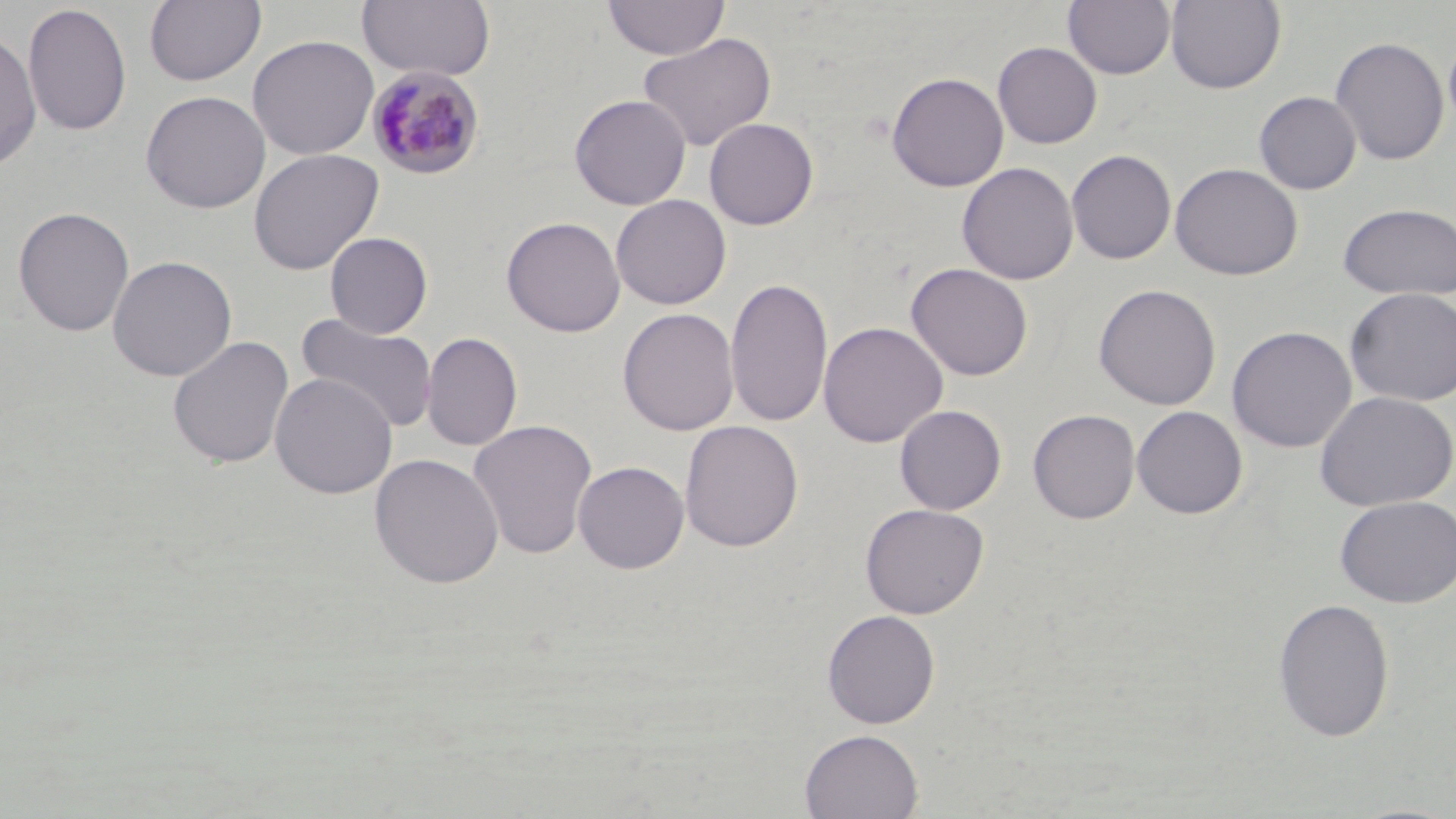
Summary:
  - Coordinate format: approximate bounding boxes as (x1, y1, x2, y2) in pixels
  - Plasmodium malariae-infected red blood cell locations: (367, 67, 484, 180)
  - Uninfected red blood cell locations: (144, 0, 266, 87), (357, 0, 496, 83), (603, 0, 729, 60), (1063, 0, 1175, 80), (1166, 0, 1286, 94), (22, 2, 132, 137), (1443, 29, 1456, 135), (0, 30, 42, 174), (637, 33, 776, 152), (247, 34, 379, 159), (1329, 36, 1450, 166), (993, 42, 1102, 148), (886, 71, 1009, 192), (140, 90, 271, 213), (1254, 91, 1361, 195), (569, 94, 691, 210), (704, 117, 818, 230), (248, 148, 384, 275), (1067, 149, 1177, 265), (957, 162, 1078, 285), (1169, 162, 1304, 281), (610, 194, 731, 310), (1337, 202, 1456, 300), (12, 206, 135, 337), (501, 216, 626, 338), (325, 232, 433, 338), (107, 255, 237, 382), (906, 263, 1034, 381), (725, 276, 833, 429), (1093, 283, 1222, 411), (1344, 288, 1456, 407), (617, 307, 739, 436), (295, 312, 439, 434), (818, 321, 947, 448), (1226, 325, 1357, 453), (421, 331, 523, 452), (167, 335, 295, 470), (270, 373, 398, 499), (1314, 390, 1456, 511), (894, 404, 1007, 515), (1131, 406, 1247, 520), (1027, 409, 1140, 524), (468, 418, 598, 560), (679, 420, 804, 552), (572, 447, 804, 566), (369, 452, 505, 589), (572, 460, 690, 574), (1335, 495, 1456, 608), (860, 503, 989, 618), (1272, 597, 1395, 743), (821, 609, 940, 729), (799, 729, 924, 818)
  - Slide-level diagnosis: Plasmodium malariae
  - Preparation: thin blood smear
  - Image size: 1456×819 pixels
  - Magnification: 1000x
  - Stain: May-Grünwald-Giemsa
  - Field of view: one of a larger specimen
  - Modality: light microscopy